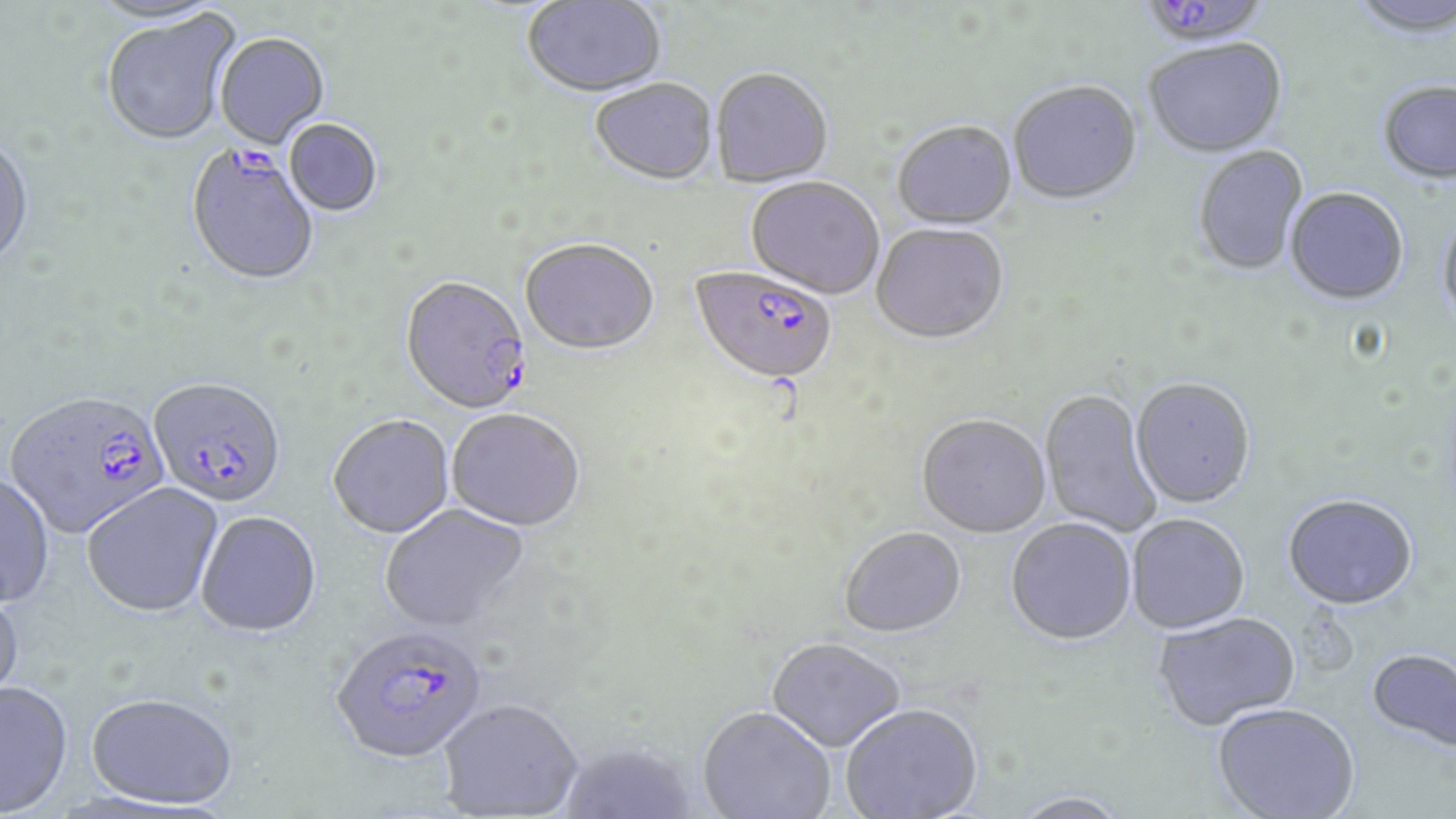
Approximate bounding boxes as (x1, y1, x2, y2) in pixels. Plasmodium falciparum-infected red blood cell locations: (1153, 0, 1263, 45), (184, 146, 320, 289), (689, 269, 836, 389), (400, 278, 533, 417), (149, 378, 287, 509), (4, 391, 170, 539), (329, 626, 487, 766). Uninfected red blood cell locations: (1348, 0, 1456, 42), (523, 1, 666, 100), (101, 10, 241, 147), (215, 34, 330, 152), (1144, 41, 1288, 160), (710, 71, 833, 190), (590, 81, 718, 188), (1008, 82, 1142, 208), (1378, 82, 1456, 187), (284, 121, 382, 218), (892, 123, 1017, 231), (0, 135, 35, 274), (1193, 146, 1309, 277), (745, 178, 883, 302), (1285, 189, 1409, 308), (1436, 213, 1456, 334), (871, 226, 1010, 347), (520, 241, 658, 359), (1130, 380, 1256, 511), (1040, 389, 1162, 537), (447, 412, 585, 534), (328, 416, 454, 540), (916, 416, 1051, 541), (0, 473, 55, 608), (82, 483, 223, 618), (1282, 496, 1418, 613), (380, 505, 530, 634), (196, 513, 322, 639), (1126, 516, 1250, 636), (1005, 519, 1136, 648), (840, 529, 966, 640), (0, 584, 25, 715), (1153, 613, 1300, 733), (767, 640, 905, 754), (1366, 649, 1456, 758), (0, 680, 73, 817), (86, 692, 239, 810), (438, 701, 582, 819), (841, 706, 983, 819), (1212, 706, 1360, 819), (697, 709, 835, 819), (557, 744, 697, 819), (1008, 794, 1133, 819). Slide-level diagnosis: Plasmodium falciparum. Image is 1456×819 pixels. Captured at 1000x magnification. Light microscopy. Thin blood film. May-Grünwald-Giemsa stain. Single field of view.